Name the parasite shown.
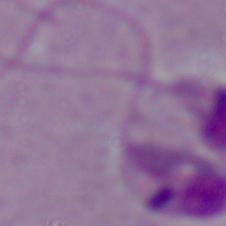

Leishmania.

magnification = 1000x
modality = micrograph